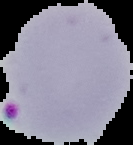
Summary:
  - Preparation: thin blood smear
  - Image size: 133×145 pixels
  - Result: malaria parasites identified
  - Image type: cell region segmented out of the field of view; surrounding area masked to black